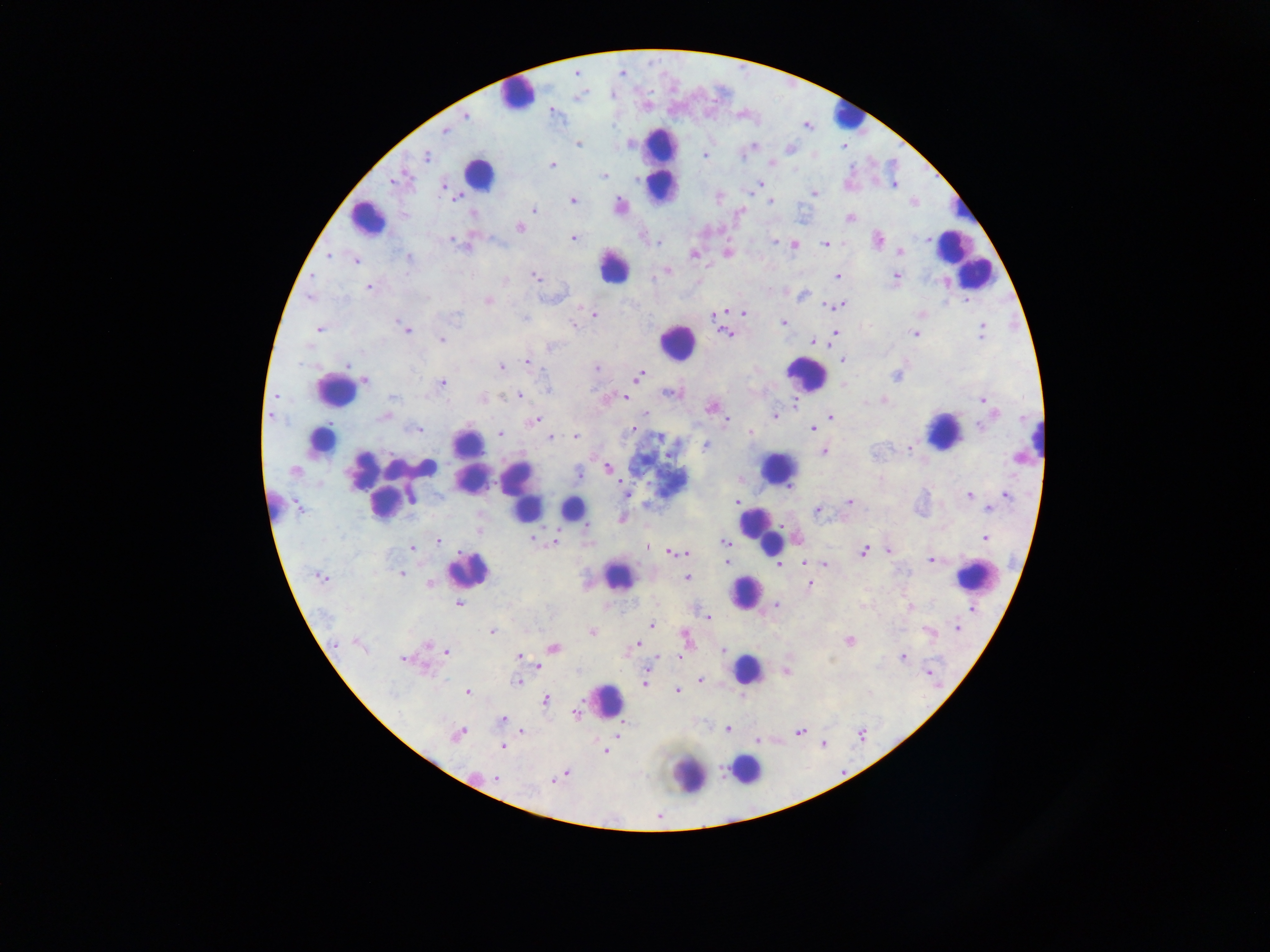 Approximate centers as {x, y} in pixels. Plasmodium parasite locations: {466, 115}, {444, 132}, {579, 144}, {629, 144}, {754, 146}, {704, 155}, {742, 155}, {426, 156}, {772, 163}, {552, 165}, {603, 176}, {396, 180}, {760, 184}, {894, 185}, {443, 187}, {815, 193}, {457, 198}, {573, 200}, {771, 202}, {914, 203}, {620, 205}, {535, 210}, {472, 215}, {855, 217}, {520, 228}, {573, 238}, {878, 239}, {927, 239}, {451, 240}, {775, 241}, {656, 242}, {778, 243}, {825, 244}, {795, 245}, {463, 247}, {901, 251}, {727, 253}, {329, 255}, {693, 255}, {409, 258}, {355, 260}, {667, 271}, {837, 276}, {895, 277}, {536, 278}, {369, 288}, {803, 295}, {488, 300}, {966, 300}, {829, 305}, {840, 306}, {744, 312}, {714, 314}, {594, 315}, {524, 319}, {783, 322}, {572, 325}, {319, 329}, {407, 329}, {982, 330}, {915, 333}, {726, 334}, {835, 334}, {441, 340}, {814, 341}, {550, 348}, {843, 361}, {527, 362}, {347, 366}, {501, 367}, {597, 367}, {640, 375}, {896, 376}, {366, 381}, {442, 383}, {547, 389}, {671, 393}, {276, 396}, {518, 396}, {392, 398}, {624, 398}, {982, 400}, {884, 401}, {795, 402}, {711, 407}, {645, 415}, {270, 416}, {774, 416}, {382, 417}, {831, 417}, {534, 420}, {728, 420}, {982, 426}, {632, 429}, {812, 429}, {416, 430}, {751, 432}, {500, 434}, {575, 437}, {551, 438}, {660, 439}, {705, 446}, {909, 448}, {824, 451}, {299, 468}, {609, 469}, {579, 473}, {625, 493}, {970, 495}, {1006, 495}, {411, 499}, {736, 501}, {301, 502}, {849, 502}, {988, 508}, {817, 510}, {587, 526}, {985, 538}, {533, 539}, {438, 541}, {555, 542}, {725, 542}, {648, 547}, {413, 548}, {889, 551}, {675, 552}, {864, 552}, {931, 561}, {727, 563}, {805, 563}, {780, 565}, {824, 565}, {401, 574}, {319, 577}, {687, 578}, {430, 584}, {810, 585}, {458, 604}, {776, 605}, {909, 607}, {973, 608}, {708, 617}, {651, 625}, {957, 627}, {492, 632}, {592, 632}, {930, 632}, {686, 637}, {849, 640}, {335, 644}, {636, 644}, {428, 645}, {554, 648}, {723, 650}, {447, 652}, {519, 657}, {679, 657}, {902, 657}, {403, 659}, {539, 667}, {929, 671}, {701, 680}, {517, 682}, {645, 682}, {677, 691}, {467, 692}, {546, 700}, {576, 713}, {502, 719}, {727, 729}, {522, 731}, {800, 731}, {457, 734}, {617, 735}, {757, 740}, {822, 743}, {502, 746}, {605, 751}, {566, 773}, {496, 778}, {554, 780}. Leukocyte locations (subset; some below the resolvable size): {517, 93}, {846, 115}, {662, 164}, {480, 172}, {966, 207}, {368, 218}, {953, 247}, {963, 259}, {614, 267}, {677, 342}, {805, 374}, {336, 390}, {943, 430}, {328, 434}, {1030, 437}, {470, 456}, {430, 467}, {400, 468}, {778, 468}, {521, 489}, {383, 504}, {273, 507}, {572, 508}, {762, 531}, {469, 568}, {975, 576}, {617, 578}, {745, 591}, {746, 668}, {607, 699}, {745, 770}, {689, 775}. Image is 1270×952 pixels. One field of view. Thick blood smear. Sample from Ghana. Photographed through a microscope with a mobile-phone camera.